State the preparation type.
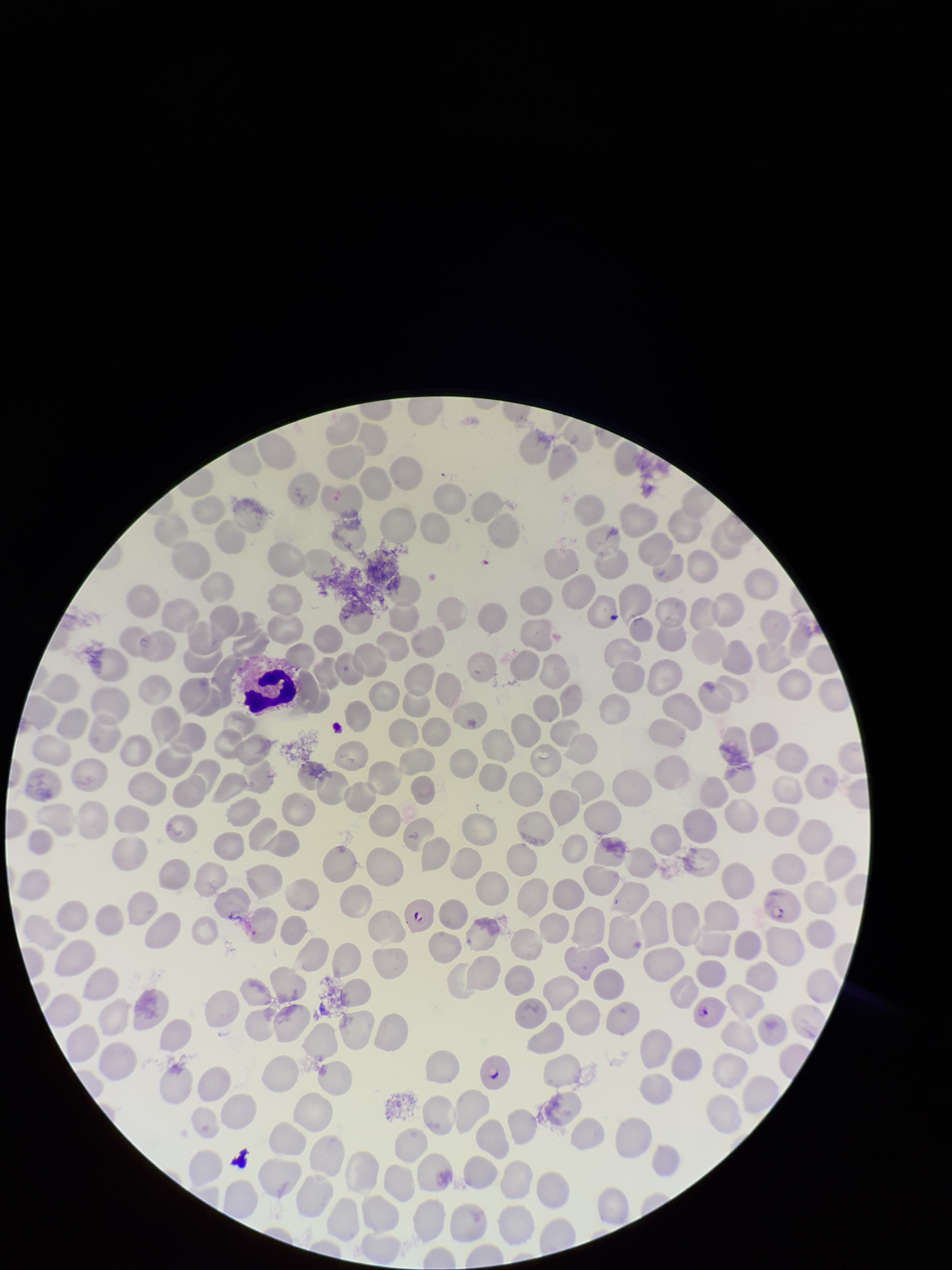
A thin smear.

Summary:
  - Image size: 952×1270 pixels
  - Parasitized red blood cell count: 4
  - Patient malaria status: infected
  - Species reported for this patient: Plasmodium falciparum
  - Field of view: single
  - Capture: smartphone photograph through the microscope eyepiece
  - Parasitized red blood cells: seen
  - Stain: Giemsa
  - Red blood cell count: 239